Give the extent of all Plasmodium vivax-infected red blood cells.
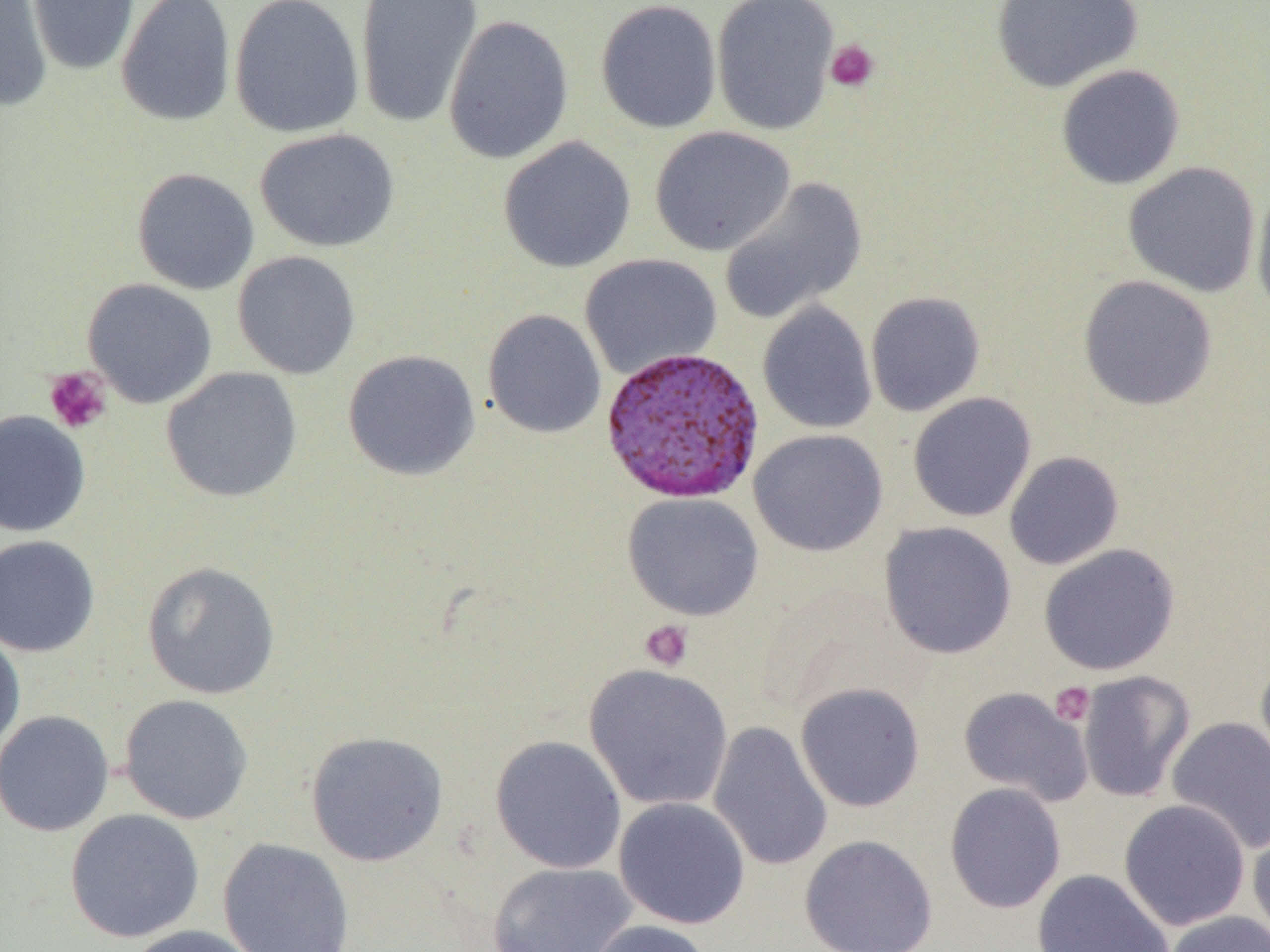
Approximate bounding boxes as named x1/y1/x2/y2 corners in pixels.
Plasmodium vivax-infected red blood cells: (x1=600, y1=346, x2=766, y2=504).

Uninfected red blood cell locations: (x1=0, y1=0, x2=52, y2=112), (x1=26, y1=0, x2=140, y2=76), (x1=116, y1=0, x2=236, y2=127), (x1=229, y1=0, x2=364, y2=138), (x1=354, y1=0, x2=483, y2=128), (x1=595, y1=0, x2=722, y2=134), (x1=711, y1=0, x2=840, y2=136), (x1=990, y1=0, x2=1144, y2=92), (x1=443, y1=14, x2=574, y2=165), (x1=1055, y1=64, x2=1186, y2=190), (x1=649, y1=126, x2=796, y2=256), (x1=254, y1=128, x2=400, y2=252), (x1=498, y1=136, x2=636, y2=273), (x1=1122, y1=161, x2=1262, y2=297), (x1=131, y1=167, x2=260, y2=295), (x1=719, y1=176, x2=867, y2=326), (x1=1251, y1=184, x2=1270, y2=321), (x1=232, y1=250, x2=361, y2=379), (x1=580, y1=254, x2=722, y2=379), (x1=1078, y1=275, x2=1218, y2=411), (x1=82, y1=278, x2=217, y2=408), (x1=865, y1=291, x2=986, y2=417), (x1=757, y1=301, x2=877, y2=434), (x1=482, y1=309, x2=607, y2=439), (x1=342, y1=349, x2=481, y2=481), (x1=161, y1=367, x2=302, y2=502), (x1=907, y1=392, x2=1037, y2=522), (x1=0, y1=409, x2=90, y2=537), (x1=748, y1=428, x2=888, y2=557), (x1=1004, y1=451, x2=1125, y2=570), (x1=622, y1=492, x2=765, y2=621), (x1=879, y1=521, x2=1016, y2=659), (x1=0, y1=535, x2=101, y2=657), (x1=1038, y1=544, x2=1180, y2=675), (x1=142, y1=561, x2=281, y2=700), (x1=0, y1=628, x2=25, y2=757), (x1=1254, y1=653, x2=1270, y2=785), (x1=584, y1=663, x2=733, y2=811), (x1=1077, y1=670, x2=1196, y2=803), (x1=795, y1=682, x2=926, y2=812), (x1=958, y1=687, x2=1093, y2=806), (x1=118, y1=693, x2=254, y2=825), (x1=0, y1=709, x2=114, y2=837), (x1=1166, y1=716, x2=1270, y2=854), (x1=708, y1=721, x2=833, y2=871), (x1=305, y1=730, x2=449, y2=867), (x1=489, y1=735, x2=627, y2=874), (x1=944, y1=783, x2=1066, y2=913), (x1=613, y1=797, x2=751, y2=929), (x1=1119, y1=798, x2=1251, y2=931), (x1=64, y1=808, x2=205, y2=943), (x1=1247, y1=818, x2=1270, y2=946), (x1=799, y1=834, x2=938, y2=952), (x1=217, y1=837, x2=356, y2=952), (x1=487, y1=862, x2=638, y2=952), (x1=1031, y1=869, x2=1174, y2=952), (x1=1163, y1=910, x2=1270, y2=952), (x1=585, y1=919, x2=713, y2=952), (x1=127, y1=924, x2=264, y2=952). Platelet locations: (x1=824, y1=39, x2=880, y2=92), (x1=43, y1=367, x2=112, y2=434), (x1=640, y1=619, x2=694, y2=672), (x1=1049, y1=681, x2=1095, y2=727). Slide-level diagnosis: Plasmodium vivax. Captured at 1000x magnification. Single field of view. Image is 1270×952 pixels. Optical microscopy. Thin blood smear.